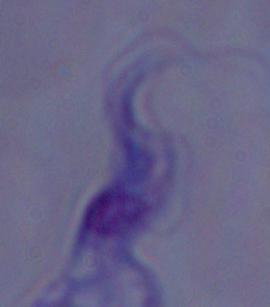

Photomicrograph. A trypanosome is seen. Captured at 1000x magnification.